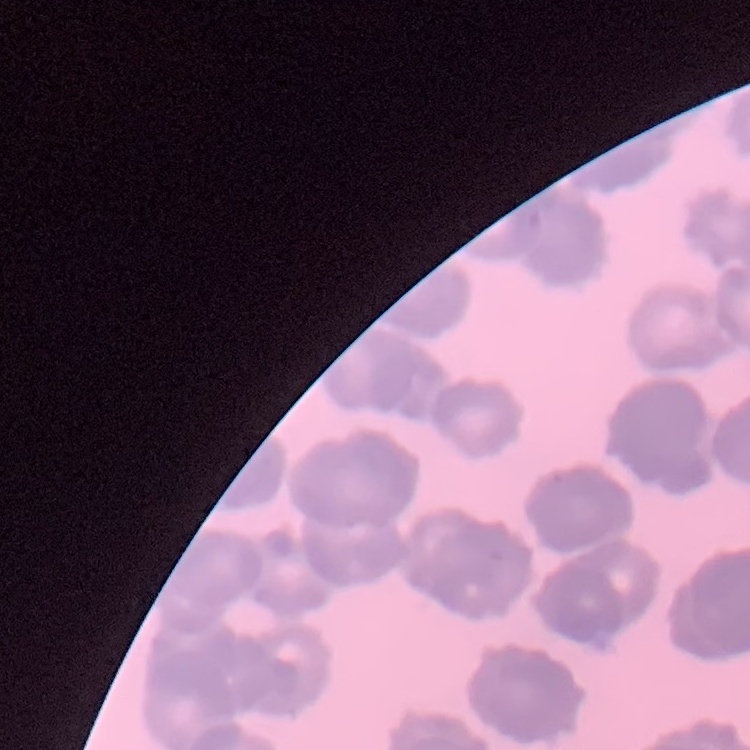

The erythrocytes exhibit rouleaux formation. One tile cut from a larger photomicrograph. Field's or Giemsa stain. Thin peripheral smear.